State which parasite is depicted.
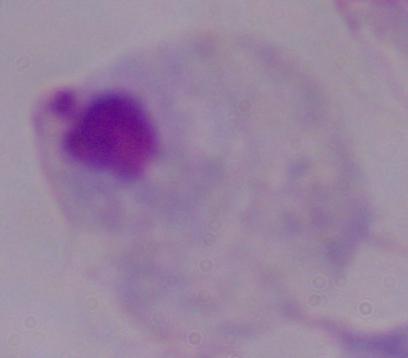
This is a trichomonad.

modality = micrograph
magnification = 1000x